Locate every blood parasite and identify its species.
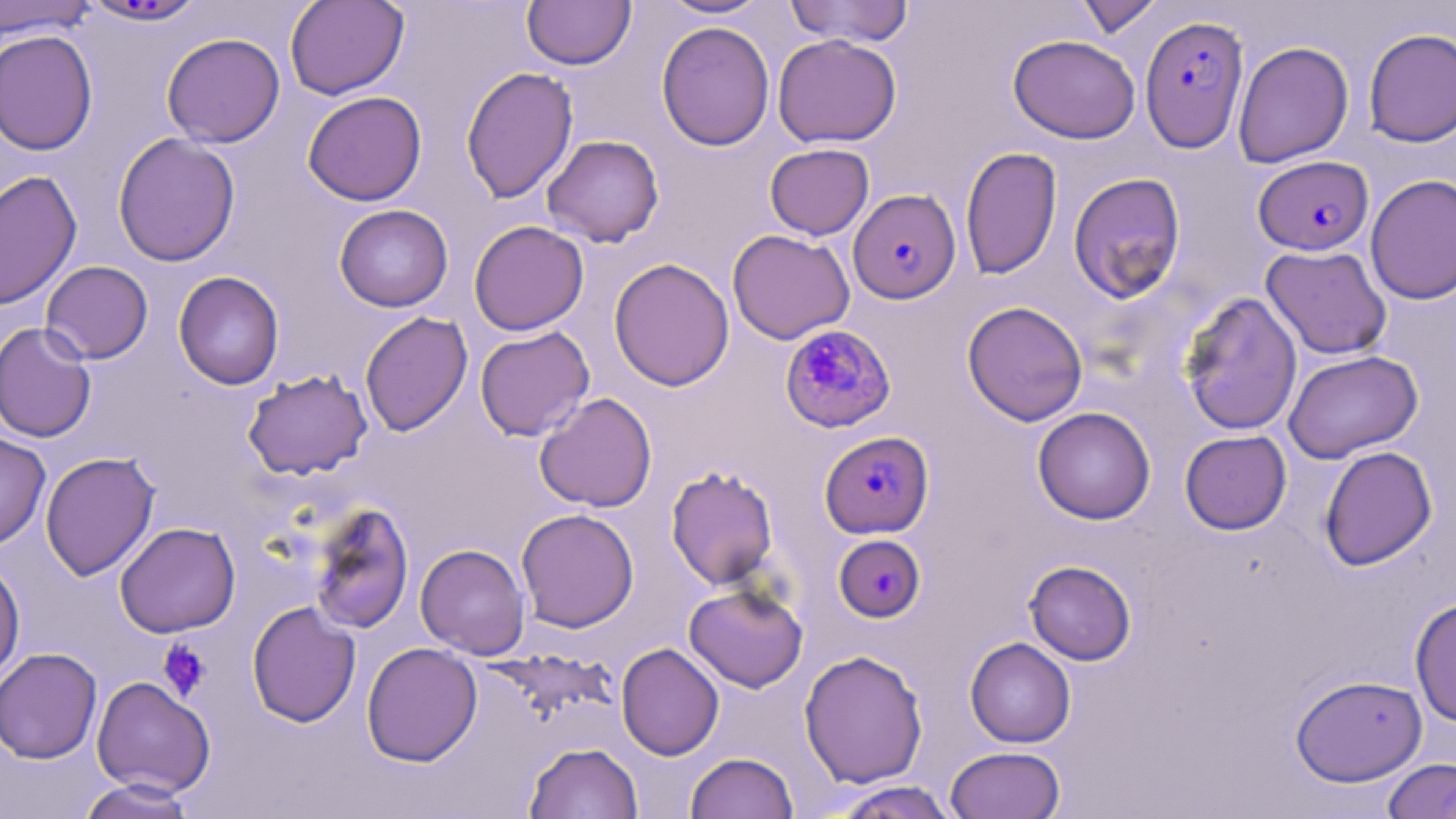

Approximate bounding boxes as (x1, y1, x2, y2) in pixels.
Plasmodium falciparum-infected red blood cells: (1139, 14, 1250, 153), (1253, 155, 1374, 256), (848, 188, 961, 304), (779, 324, 897, 433), (819, 430, 934, 539), (833, 534, 926, 622).
No Plasmodium ovale, Plasmodium malariae, Plasmodium vivax, Babesia divergens, or Trypanosoma brucei observed.

Summary:
  - Platelet locations: (157, 639, 213, 701)
  - Uninfected red blood cell locations: (285, 0, 409, 100), (522, 0, 636, 70), (659, 0, 771, 19), (784, 0, 915, 47), (1074, 0, 1163, 38), (0, 1, 99, 40), (79, 1, 209, 28), (656, 21, 775, 151), (1363, 28, 1456, 147), (0, 29, 99, 156), (161, 32, 285, 148), (773, 33, 902, 148), (1008, 34, 1140, 143), (1232, 41, 1353, 168), (460, 66, 579, 205), (302, 90, 427, 206), (113, 132, 240, 267), (542, 134, 665, 247), (764, 143, 874, 240), (960, 146, 1062, 280), (0, 170, 82, 309), (1068, 172, 1186, 303), (1365, 174, 1456, 305), (334, 204, 453, 312), (469, 220, 589, 336), (727, 229, 855, 344), (1260, 245, 1392, 360), (608, 257, 735, 392), (40, 260, 154, 364), (173, 270, 285, 390), (1179, 291, 1303, 436), (962, 300, 1088, 426), (360, 311, 473, 437), (0, 322, 97, 443), (475, 326, 595, 441), (1283, 349, 1423, 464), (242, 368, 373, 480), (534, 392, 657, 513), (1032, 407, 1156, 524), (1180, 430, 1292, 535), (0, 431, 51, 551), (1319, 445, 1437, 571), (40, 451, 161, 581), (665, 464, 779, 590), (307, 502, 415, 634), (515, 508, 639, 633), (115, 521, 240, 638), (415, 543, 531, 659), (0, 557, 26, 685), (1024, 560, 1136, 665), (683, 582, 809, 692), (1409, 595, 1456, 727), (246, 601, 361, 727), (964, 637, 1076, 748), (361, 642, 482, 767), (616, 642, 724, 761), (0, 647, 102, 764), (799, 649, 928, 788), (1290, 674, 1427, 786), (92, 676, 216, 797), (523, 741, 644, 818), (945, 746, 1066, 819), (685, 752, 799, 819), (1383, 758, 1455, 819), (76, 778, 199, 818), (828, 781, 960, 819)
  - Slide-level diagnosis: Plasmodium falciparum
  - Modality: light microscopy
  - Stain: May-Grünwald-Giemsa
  - Preparation: thin blood smear
  - Image size: 1456×819 pixels
  - Magnification: 1000x
  - Field of view: single